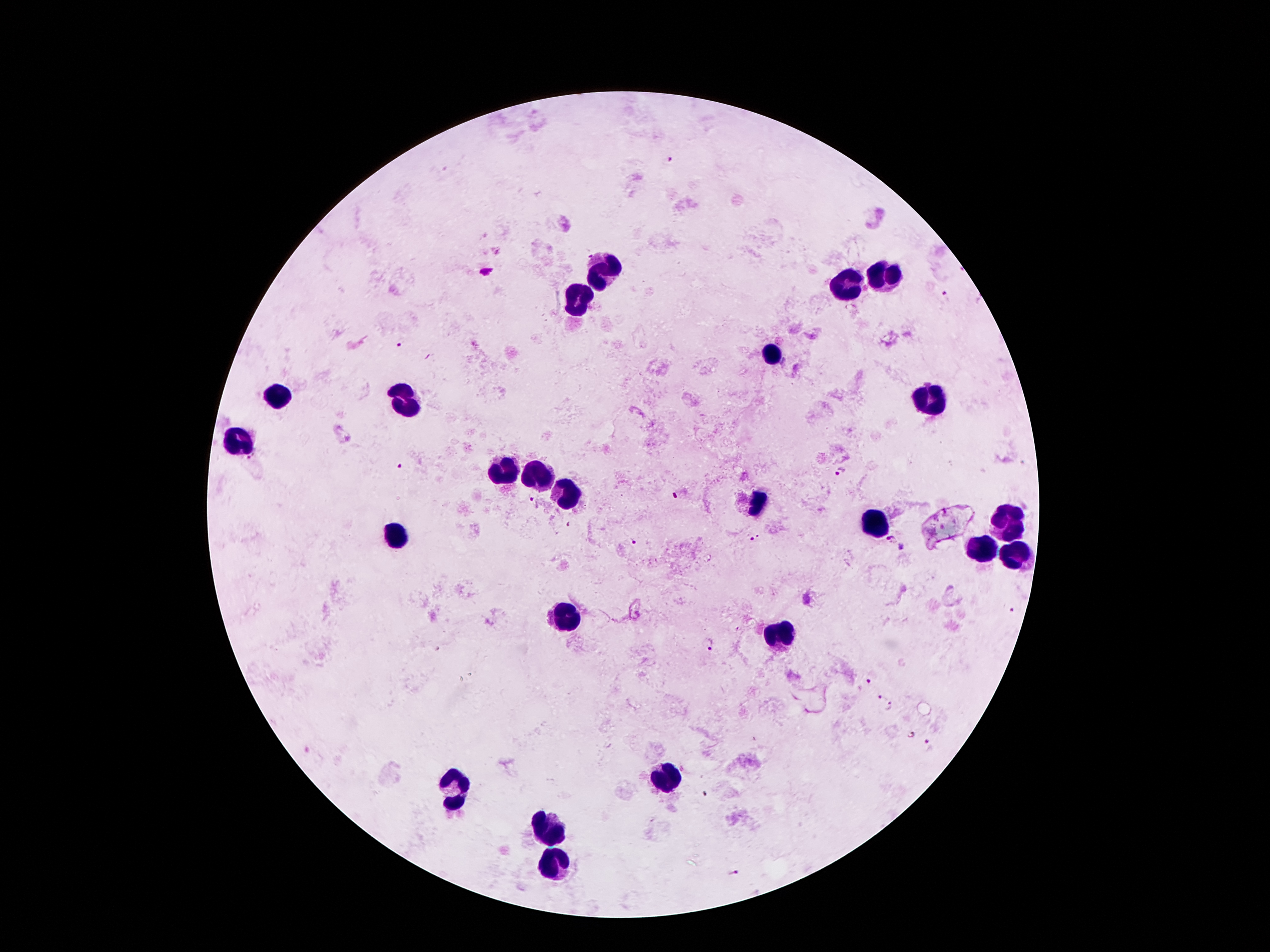

{
  "capture": "smartphone through the microscope eyepiece",
  "field_of_view": "one from this slide",
  "preparation": "thick blood film",
  "magnification": "100x",
  "patient_malaria_status": "positive for Plasmodium falciparum",
  "image_size": "1270×952 pixels",
  "stain": "Giemsa",
  "leukocyte_locations": "approximate centers as (x, y) in pixels: (601, 271), (888, 279), (850, 285), (580, 300), (773, 355), (279, 399), (932, 399), (409, 407), (237, 439), (504, 472), (538, 479), (569, 497), (758, 500), (1008, 521), (880, 527), (395, 537), (979, 550), (1014, 554), (565, 621), (781, 636), (664, 781), (454, 789), (552, 827), (554, 865)",
  "plasmodium_parasite_locations": "approximate centers as (x, y) in pixels: (668, 160), (486, 271), (946, 299), (400, 343), (400, 466), (841, 475), (676, 496), (530, 498), (754, 537), (891, 541), (634, 542), (902, 549), (708, 643), (867, 680), (882, 696), (890, 707), (912, 734), (929, 744), (735, 874)"
}